Assess this cell for malaria.
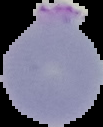
It is parasitized.

image size = 103×127 pixels
image type = cell region segmented out of the field of view; surrounding area masked to black
preparation = thin blood film